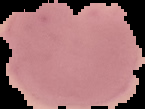
image size = 145×109 pixels
malaria status = parasitized
image type = segmented cell region on a black background
preparation = thin blood film